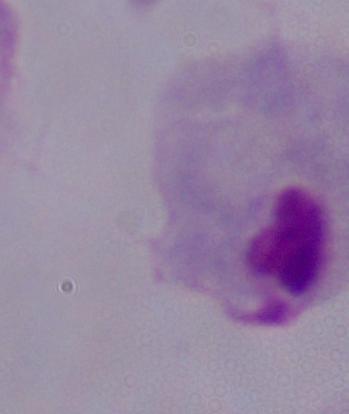

Summary:
  - Modality: micrograph
  - Identification: trichomonad
  - Magnification: 1000x